State the blood parasite species.
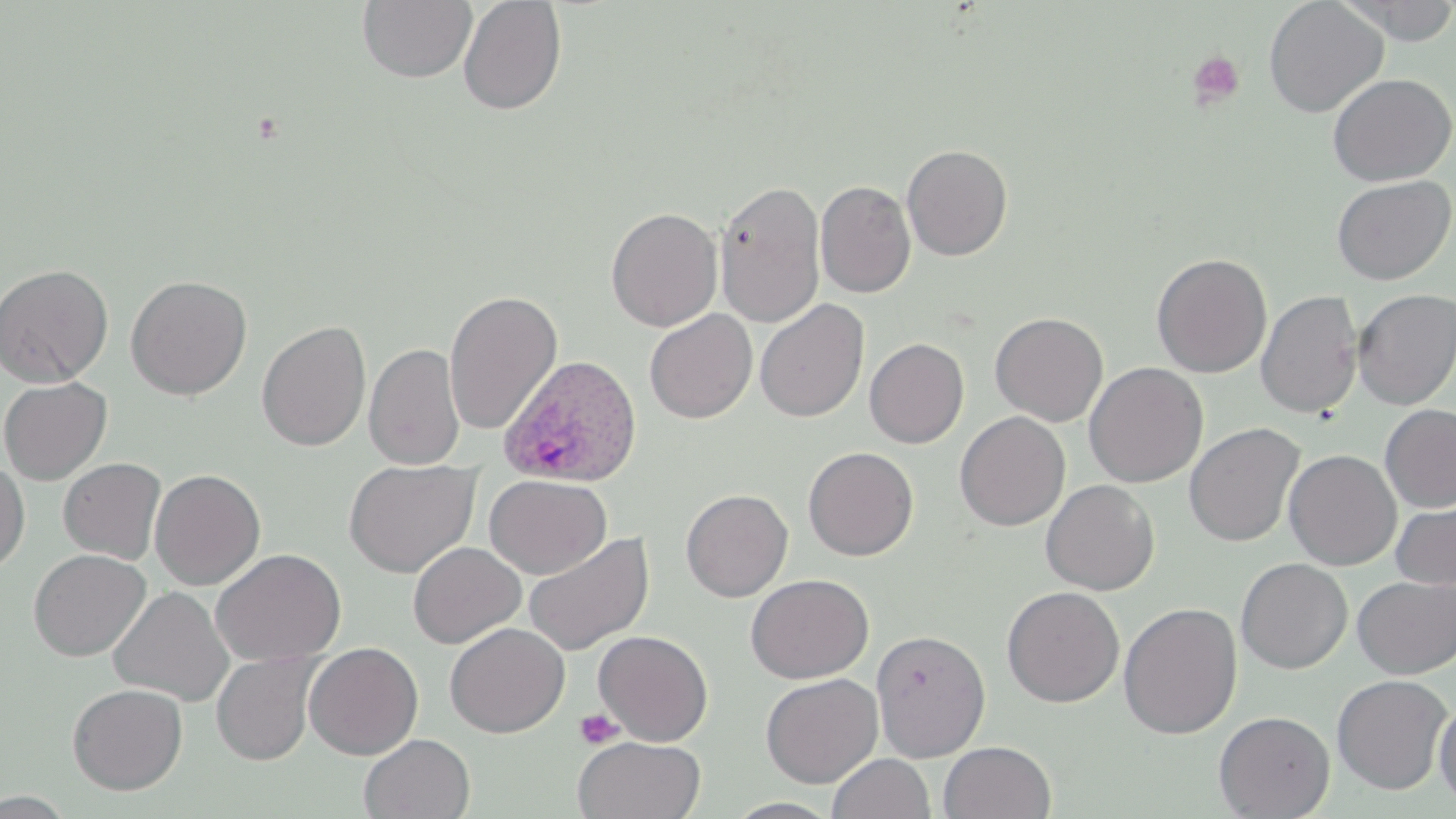
Plasmodium ovale.

Summary:
  - Coordinate format: approximate bounding boxes as [x1, y1, x2, y2] in pixels
  - Plasmodium ovale-infected red blood cell locations: [499, 354, 643, 488]
  - Uninfected red blood cell locations: [358, 0, 476, 84], [1263, 0, 1388, 117], [1339, 0, 1456, 45], [458, 1, 567, 116], [1327, 73, 1455, 186], [902, 144, 1013, 261], [1331, 175, 1454, 286], [714, 180, 825, 327], [815, 180, 916, 298], [606, 206, 723, 331], [1151, 252, 1273, 378], [0, 263, 114, 388], [125, 275, 252, 400], [1352, 289, 1456, 409], [444, 290, 562, 435], [1256, 290, 1363, 419], [755, 299, 869, 422], [644, 309, 758, 424], [990, 312, 1108, 426], [256, 320, 371, 452], [865, 337, 969, 448], [364, 343, 465, 470], [1084, 362, 1208, 488], [0, 376, 112, 485], [1379, 404, 1456, 513], [955, 411, 1070, 531], [1184, 422, 1305, 547], [803, 446, 918, 561], [1283, 449, 1401, 570], [58, 457, 166, 564], [343, 458, 480, 578], [0, 459, 30, 575], [149, 469, 266, 590], [484, 473, 611, 579], [1041, 479, 1159, 595], [680, 488, 793, 602], [1391, 496, 1456, 591], [523, 531, 654, 656], [408, 542, 526, 648], [211, 548, 346, 666], [28, 549, 150, 661], [1235, 557, 1352, 674], [745, 573, 873, 683], [1352, 575, 1456, 679], [108, 586, 234, 706], [1002, 586, 1124, 707], [1118, 601, 1242, 739], [444, 622, 569, 738], [593, 629, 713, 746], [871, 629, 991, 761], [303, 642, 424, 759], [211, 652, 319, 765], [760, 673, 883, 788], [1331, 674, 1452, 794], [67, 683, 187, 795], [1434, 699, 1456, 810], [1214, 710, 1335, 818], [359, 733, 475, 818], [573, 735, 706, 819], [939, 741, 1057, 819], [828, 753, 935, 819], [0, 790, 76, 817]
  - Platelet locations: [1187, 52, 1245, 110], [574, 708, 625, 750]
  - Image size: 1456×819 pixels
  - Stain: May-Grünwald-Giemsa
  - Field of view: one of a larger specimen
  - Preparation: thin blood film
  - Magnification: 1000x
  - Modality: light microscopy